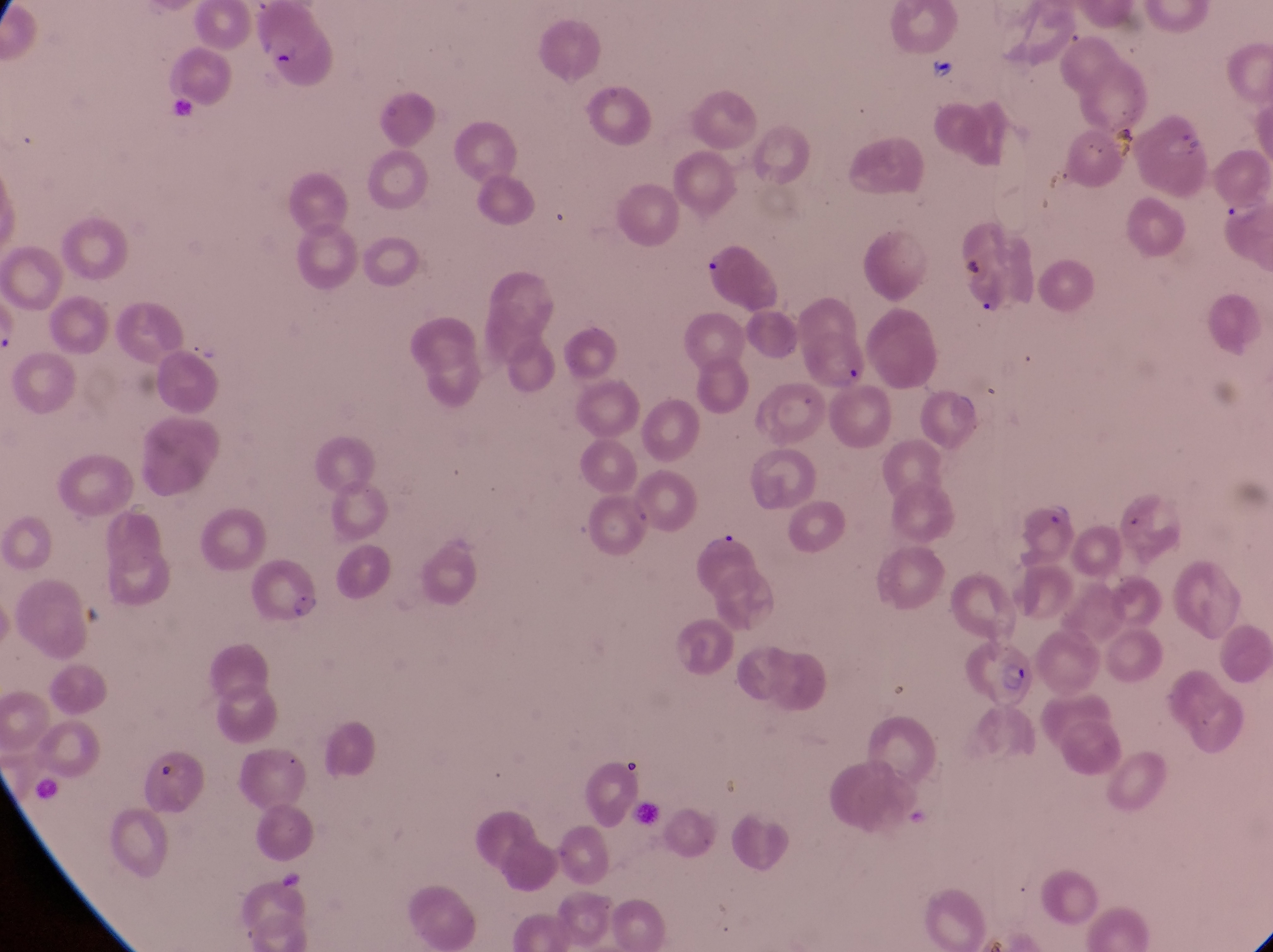
Approximate bounding boxes as (left, top, right, bottom) in pixels. Artifact (platelet-like body, stain precipitate, or debris) locations: (264, 45, 301, 77), (956, 248, 984, 287), (839, 364, 867, 396), (157, 762, 184, 789). Parasitised red blood cell locations: (697, 239, 782, 311), (1018, 492, 1081, 569), (252, 550, 319, 624), (969, 639, 1034, 719). Thin blood smear. Collected in Uganda. At a magnification of 1000x. One field of view. Captured by a smartphone held over the eyepiece of an Olympus CX-23 microscope. Image is 1273×952 pixels.